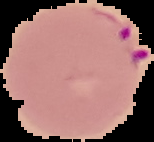
Summary:
  - Preparation: thin blood film
  - Image type: segmented cell region with the area outside set to black
  - Image size: 154×142 pixels
  - Result: malaria parasites identified